Classify this cell by malaria status.
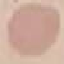

Uninfected.

Automatically extracted cell patch, resized to 64 × 64 pixels. Thin smear of blood. Giemsa stain. Acquired by smartphone through the microscope eyepiece.